Point out each Plasmodium parasite.
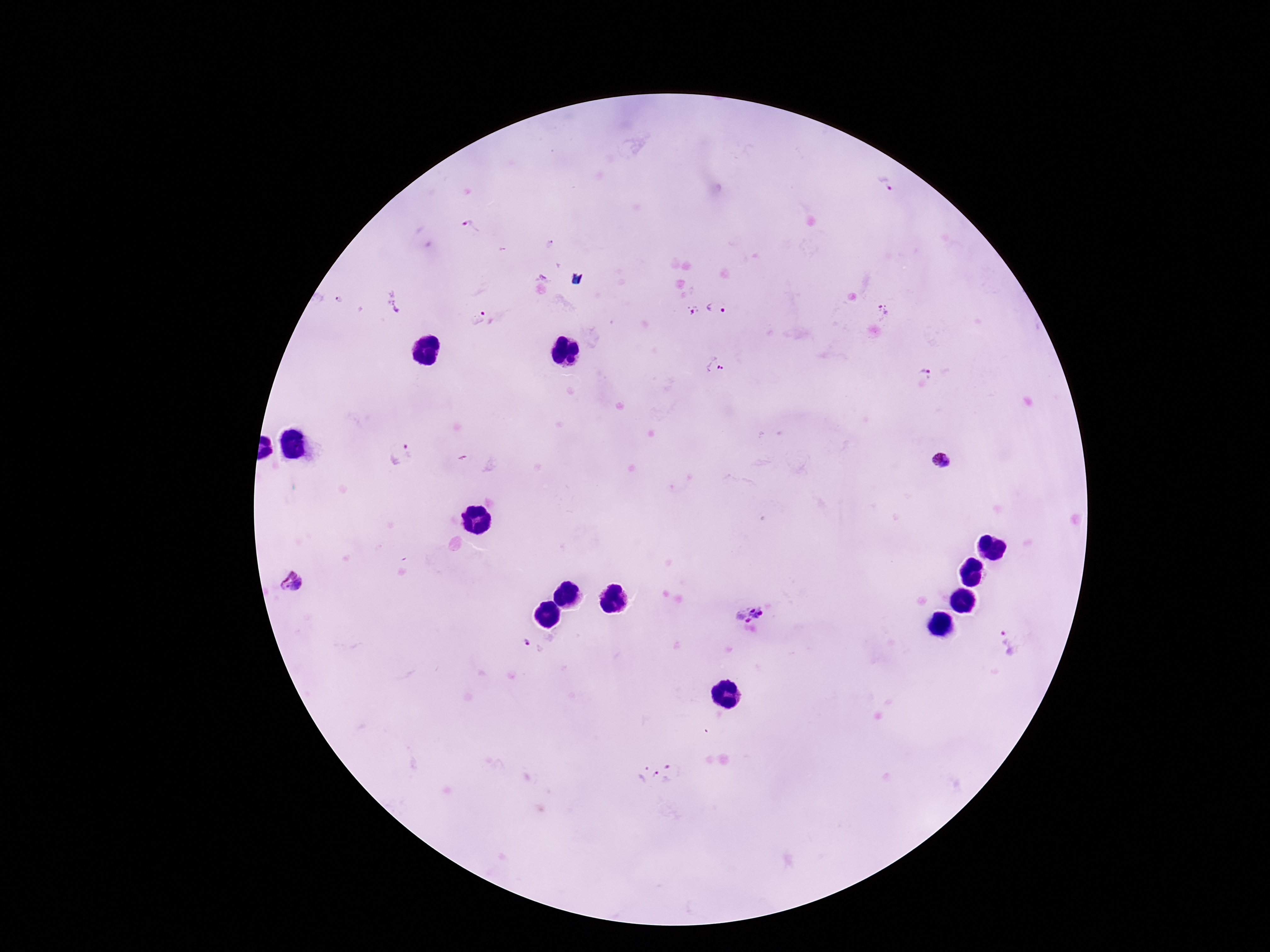

Approximate centers as {x, y} in pixels.
Plasmodium parasites: {885, 182}, {470, 227}, {338, 299}, {397, 303}, {715, 307}, {693, 310}, {884, 310}, {478, 316}, {713, 366}, {925, 371}, {399, 454}, {941, 460}, {294, 581}, {748, 608}, {1006, 643}, {532, 646}, {658, 774}.

Smartphone photograph taken through the microscope eyepiece. Image is 1270×952 pixels. 100x magnification. Thick peripheral-blood smear. Giemsa stain. One field from this slide. Patient malaria status: infected.